Point out each leukocyte.
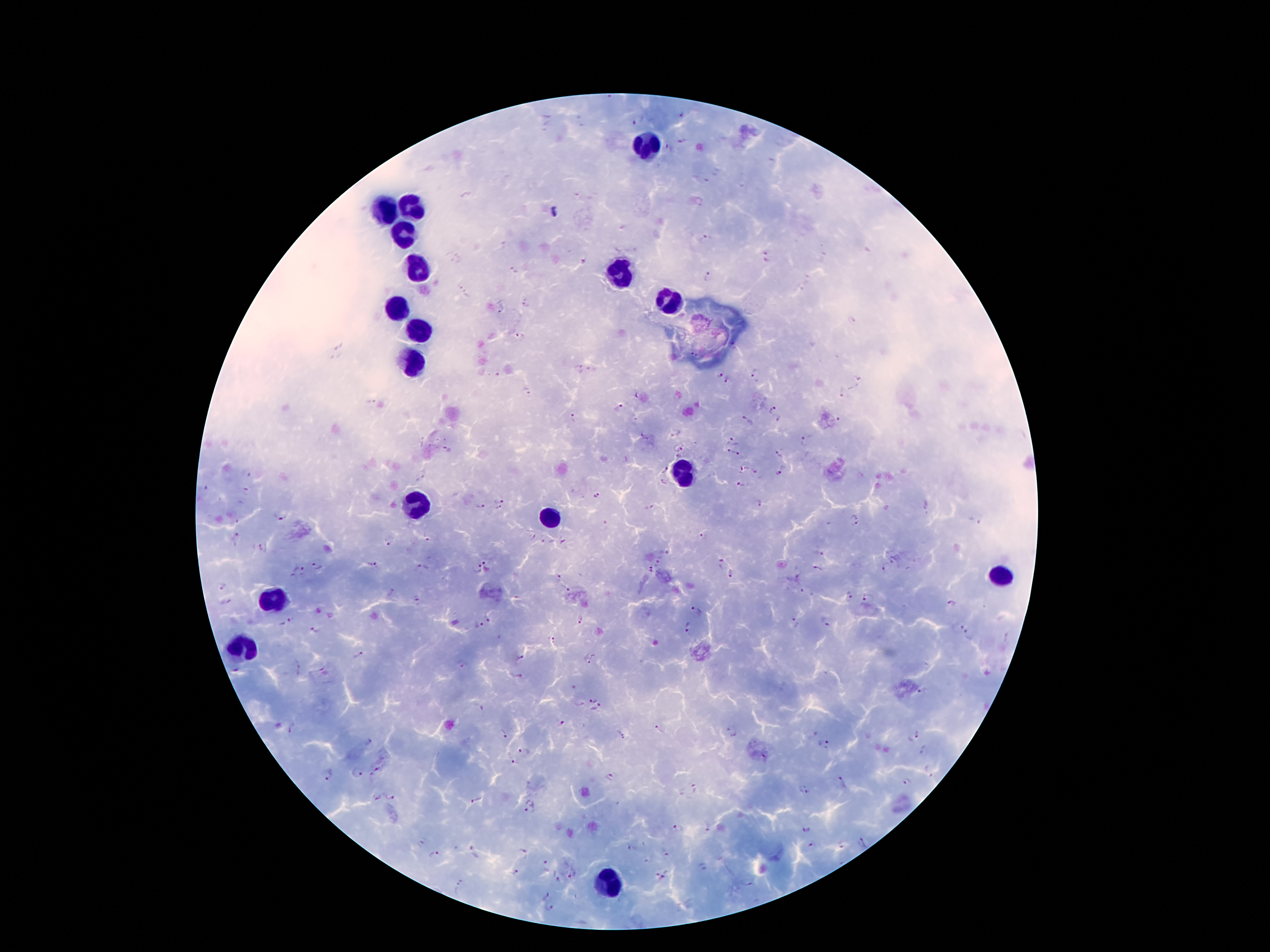

Approximate centers as [x, y] in pixels.
Leukocytes: [643, 148], [384, 208], [411, 208], [401, 232], [419, 264], [619, 274], [666, 301], [396, 306], [419, 326], [411, 363], [683, 472], [416, 506], [552, 519], [999, 576], [273, 595], [241, 645], [614, 887].

Summary:
  - Malaria parasite locations: [680, 115], [638, 119], [682, 140], [705, 239], [586, 257], [513, 269], [706, 275], [467, 295], [525, 304], [851, 319], [520, 335], [693, 354], [591, 368], [578, 369], [718, 374], [757, 375], [728, 379], [858, 379], [525, 391], [843, 394], [618, 408], [774, 411], [572, 418], [746, 418], [839, 418], [677, 431], [732, 439], [806, 439], [678, 445], [727, 450], [781, 451], [679, 455], [737, 455], [741, 468], [662, 469], [782, 469], [756, 471], [420, 475], [664, 482], [740, 486], [597, 495], [499, 499], [760, 502], [480, 505], [650, 506], [497, 510], [278, 517], [855, 519], [974, 519], [702, 535], [235, 538], [429, 539], [387, 542], [264, 546], [818, 552], [491, 563], [658, 563], [720, 563], [317, 566], [374, 567], [419, 567], [477, 567], [818, 568], [885, 568], [649, 569], [302, 573], [731, 573], [559, 577], [222, 585], [566, 589], [848, 593], [417, 598], [867, 598], [950, 603], [698, 610], [491, 617], [579, 619], [828, 621], [285, 623], [796, 623], [479, 626], [688, 626], [958, 626], [314, 631], [967, 635], [552, 640], [359, 656], [518, 657], [592, 661], [516, 675], [593, 698], [578, 703], [478, 707], [597, 708], [561, 723], [293, 730], [660, 732], [731, 732], [503, 734], [810, 734], [914, 736], [825, 745], [523, 754], [511, 762], [379, 769], [929, 770], [358, 772], [328, 774], [610, 776], [841, 781], [906, 782], [803, 789], [692, 790], [389, 797], [478, 801], [531, 808], [806, 828], [675, 830], [810, 846], [472, 852], [665, 852], [522, 853], [433, 854], [544, 866], [703, 867], [516, 875], [573, 876], [559, 877], [661, 877], [458, 887], [548, 896], [549, 907]
  - Capture: smartphone through the microscope eyepiece
  - Magnification: 100x
  - Patient malaria status: positive for Plasmodium falciparum
  - Preparation: thick blood smear
  - Stain: Giemsa
  - Image size: 1270×952 pixels
  - Field of view: single